State which parasite is depicted.
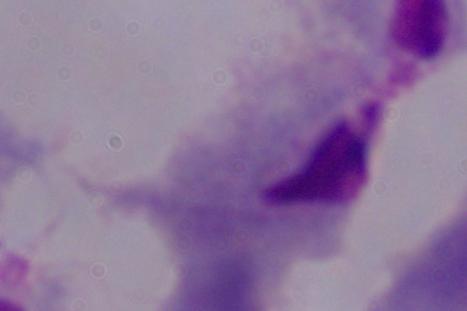
This is a trichomonad.

{
  "modality": "photomicrograph",
  "magnification": "1000x"
}